Identify the preparation type.
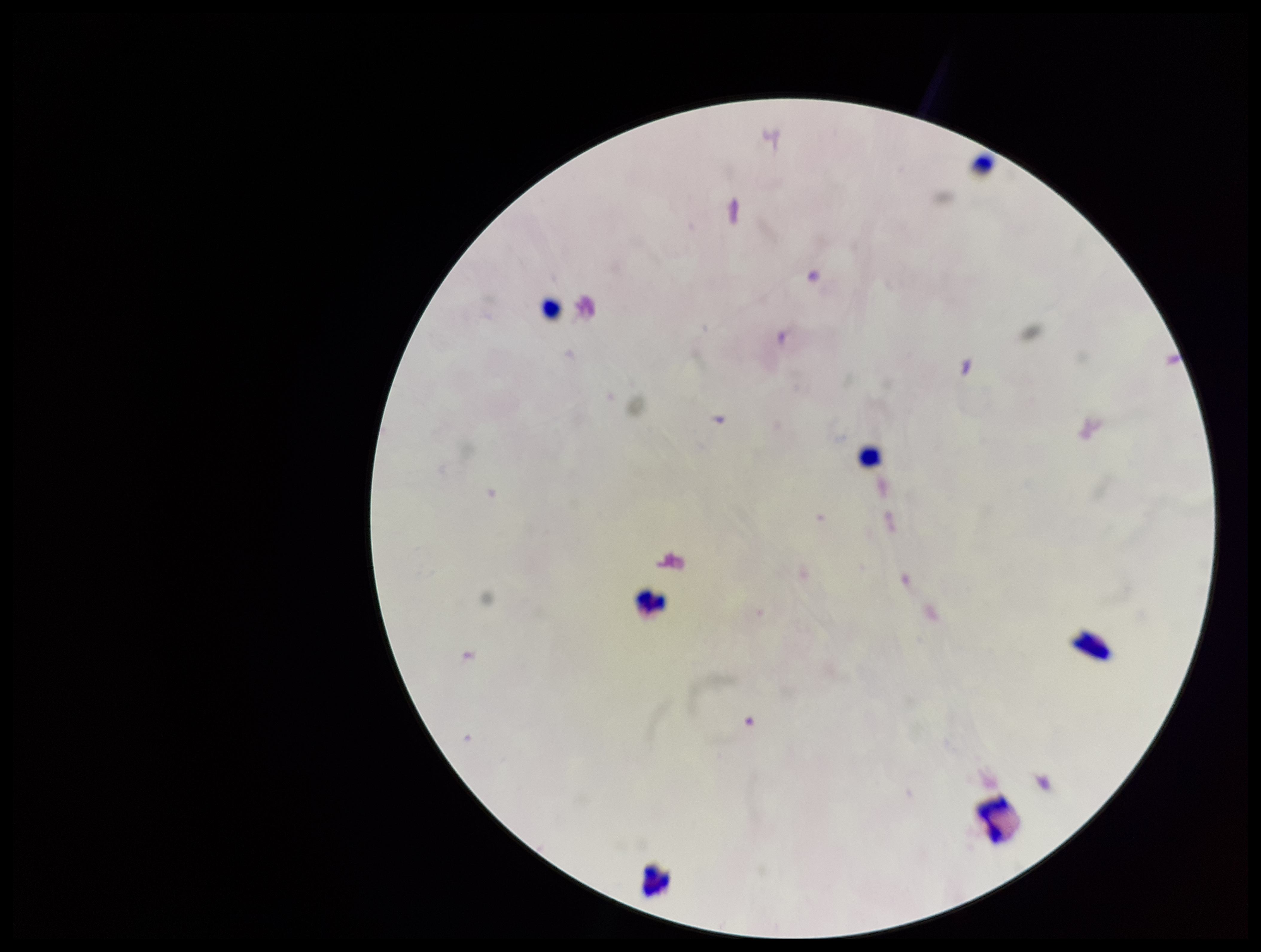

Thick.

Parasite count: 0. Single field of view. Stained with Giemsa. Leukocyte count: 6. Patient malaria status: negative. Image is 1261×952 pixels. Plasmodium parasites: none identified. Photographed through the microscope eyepiece with a smartphone camera.